Name the blood parasite species.
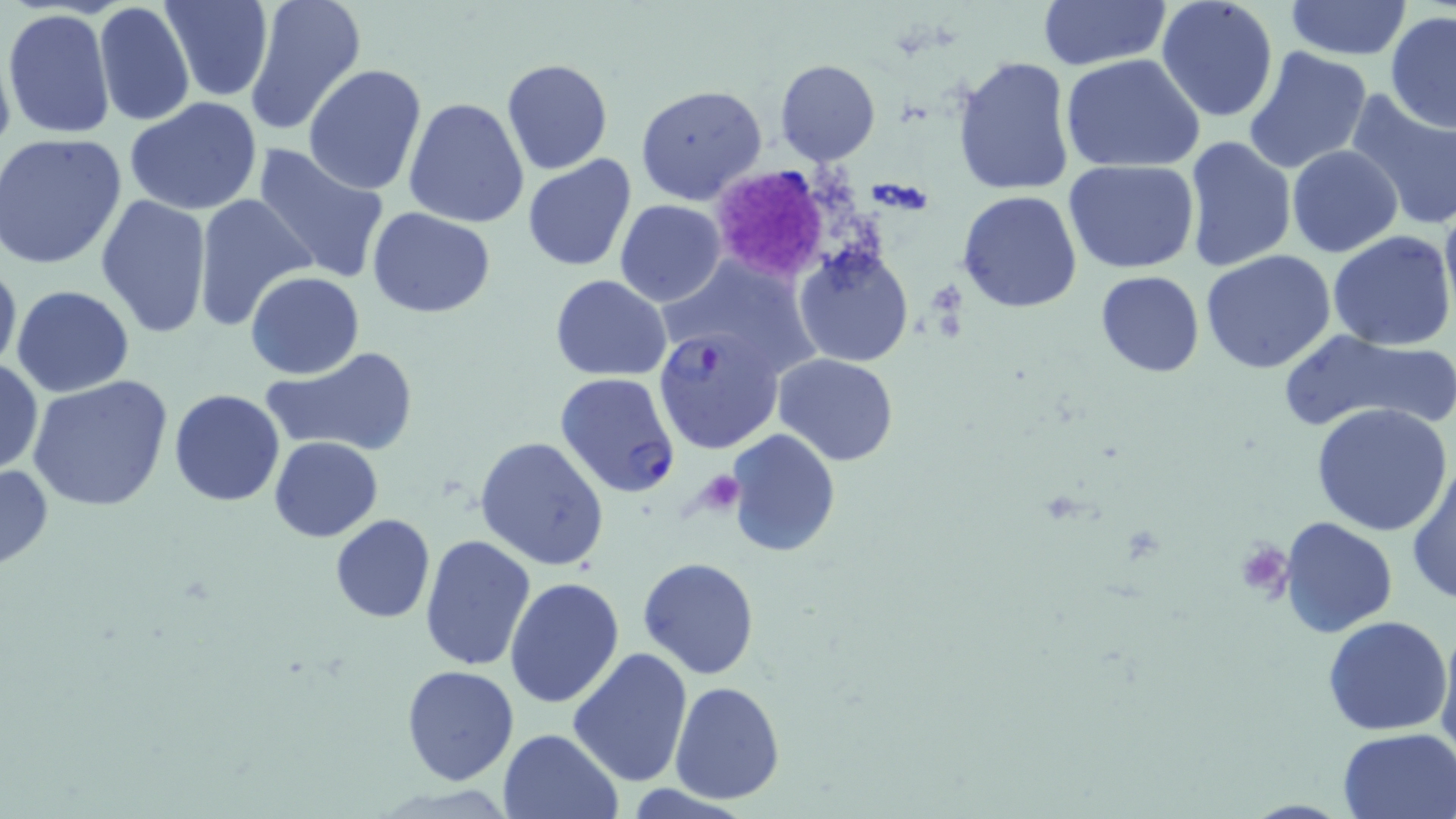
Plasmodium falciparum.

Summary:
  - Coordinate format: approximate bounding boxes as [x1, y1, x2, y2] in pixels
  - Platelet locations: [709, 163, 833, 284], [708, 471, 742, 514], [1234, 539, 1293, 602]
  - Uninfected red blood cell locations: [161, 0, 272, 103], [1156, 0, 1280, 124], [245, 1, 366, 135], [1038, 1, 1168, 73], [1284, 1, 1412, 59], [1300, 2, 1455, 88], [92, 3, 196, 127], [3, 8, 117, 143], [1385, 11, 1456, 132], [1242, 46, 1371, 176], [1061, 54, 1206, 173], [950, 56, 1075, 198], [774, 58, 880, 166], [502, 59, 612, 175], [303, 63, 428, 195], [635, 84, 767, 205], [1346, 88, 1456, 227], [403, 96, 531, 230], [123, 97, 265, 217], [1, 133, 127, 270], [1182, 135, 1298, 273], [252, 143, 392, 286], [1285, 146, 1403, 259], [522, 155, 636, 272], [1065, 160, 1201, 274], [958, 190, 1083, 313], [1440, 191, 1456, 319], [95, 194, 215, 342], [194, 194, 313, 333], [615, 198, 727, 306], [367, 208, 495, 317], [1328, 230, 1456, 351], [793, 245, 916, 367], [1200, 250, 1337, 375], [0, 252, 21, 381], [661, 256, 816, 375], [1095, 270, 1206, 376], [245, 271, 364, 380], [551, 273, 671, 381], [11, 285, 136, 398], [1281, 327, 1456, 437], [261, 346, 421, 459], [771, 354, 900, 464], [0, 359, 43, 476], [26, 375, 174, 513], [169, 389, 286, 509], [1312, 403, 1455, 537], [726, 429, 842, 556], [269, 436, 382, 542], [476, 437, 609, 571], [1408, 456, 1456, 604], [0, 459, 54, 575], [329, 514, 436, 623], [1280, 517, 1400, 638], [420, 532, 537, 671], [639, 558, 759, 678], [504, 576, 626, 708], [1436, 614, 1456, 764], [1322, 615, 1454, 736], [568, 646, 693, 786], [400, 664, 520, 786], [669, 680, 785, 804], [497, 728, 623, 818], [1336, 729, 1456, 818]
  - Plasmodium falciparum-infected red blood cell locations: [653, 325, 784, 453], [555, 372, 681, 498]
  - Modality: optical microscopy
  - Image size: 1456×819 pixels
  - Preparation: thin blood film
  - Stain: May-Grünwald-Giemsa
  - Field of view: one of a larger specimen
  - Magnification: 1000x